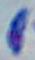
magnification = 1000x
modality = micrograph
identification = Toxoplasma gondii